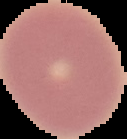 From a thin blood film. Image is 127×139 pixels. Result: negative for Plasmodium parasites. Cell region segmented out of the field of view; the surrounding area is masked to black.